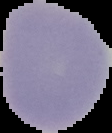

Result: no malaria parasites detected. From a thin blood smear. Image is 112×133 pixels. Cell region segmented out of the field of view; the surrounding area is masked to black.